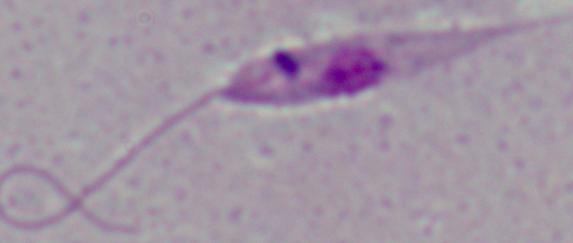

magnification = 1000x
identification = Leishmania
modality = micrograph